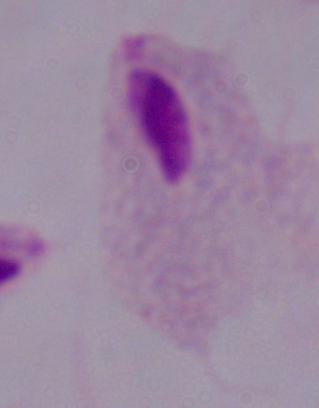
modality: micrograph
identification: trichomonad
magnification: 1000x